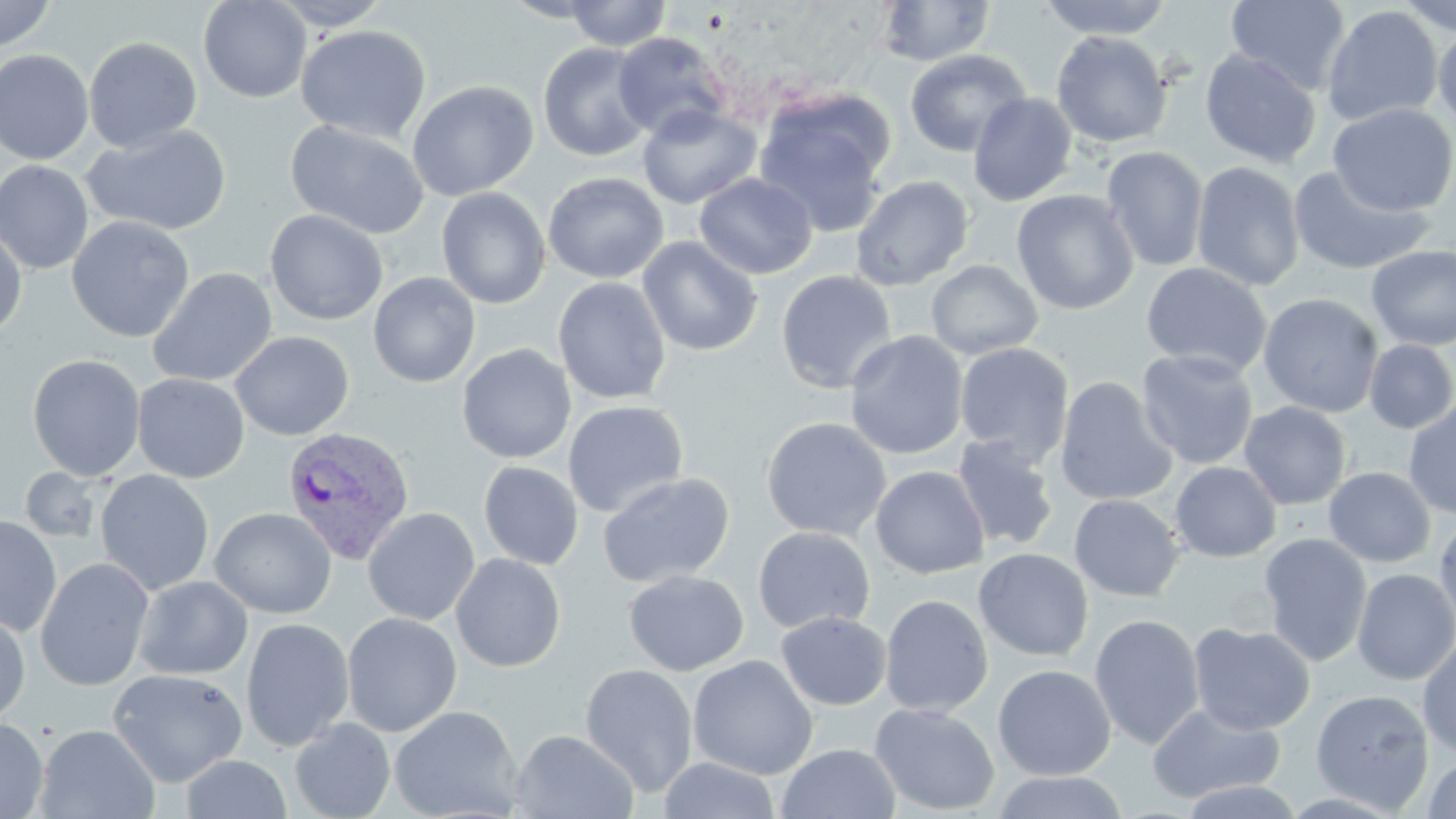
Plasmodium vivax-infected red blood cell locations = approximate bounding boxes as (x1, y1, x2, y2) in pixels: (282, 425, 415, 566)
slide-level diagnosis = Plasmodium vivax
stain = May-Grünwald-Giemsa
uninfected red blood cell locations = approximate bounding boxes as (x1, y1, x2, y2) in pixels: (0, 0, 59, 52), (198, 0, 311, 103), (268, 0, 393, 30), (562, 0, 672, 51), (1037, 0, 1174, 40), (1226, 0, 1351, 95), (1392, 0, 1456, 37), (876, 1, 997, 67), (1321, 5, 1443, 127), (1432, 21, 1456, 136), (295, 24, 432, 143), (1051, 30, 1172, 148), (612, 32, 731, 140), (83, 36, 202, 153), (537, 41, 655, 162), (904, 48, 1031, 158), (0, 49, 94, 165), (1200, 49, 1322, 168), (407, 80, 539, 201), (968, 92, 1078, 207), (753, 96, 892, 238), (637, 103, 761, 209), (1328, 103, 1456, 217), (285, 119, 431, 238), (81, 123, 232, 236), (1101, 146, 1209, 272), (0, 160, 94, 275), (1191, 161, 1305, 291), (1288, 165, 1435, 276), (543, 172, 668, 284), (694, 173, 817, 279), (850, 175, 974, 291), (436, 187, 551, 309), (1011, 189, 1139, 315), (264, 209, 388, 325), (66, 216, 195, 342), (0, 220, 28, 340), (637, 237, 763, 356), (1366, 245, 1456, 351), (926, 259, 1043, 360), (1141, 262, 1272, 377), (147, 267, 278, 387), (776, 270, 897, 394), (368, 272, 481, 388), (553, 276, 671, 404), (1258, 293, 1384, 418), (230, 330, 354, 441), (844, 330, 968, 460), (1363, 339, 1456, 434), (954, 342, 1075, 464), (457, 344, 576, 464), (1136, 349, 1259, 470), (27, 354, 145, 481), (132, 373, 249, 483), (1054, 376, 1178, 506), (562, 400, 689, 518), (1403, 400, 1456, 519), (1239, 401, 1352, 510), (760, 416, 891, 541), (949, 435, 1060, 552), (478, 460, 584, 570), (1170, 461, 1282, 562), (870, 465, 990, 579), (21, 467, 105, 544), (1323, 467, 1436, 567), (95, 469, 215, 596), (597, 472, 735, 589), (1069, 494, 1184, 602), (209, 507, 337, 619), (363, 507, 480, 625), (1434, 514, 1456, 634), (0, 516, 62, 636), (753, 526, 875, 633), (1258, 532, 1373, 666), (973, 548, 1094, 662), (450, 553, 566, 672), (35, 557, 155, 691), (1352, 568, 1456, 685), (623, 569, 749, 676), (133, 575, 253, 679), (879, 594, 993, 717), (0, 608, 30, 727), (776, 611, 891, 710), (342, 612, 462, 737), (1089, 613, 1205, 750), (240, 617, 355, 751), (1187, 622, 1315, 735), (1416, 634, 1456, 758), (688, 654, 818, 780), (579, 663, 699, 798), (993, 664, 1116, 780), (108, 668, 248, 787), (1311, 689, 1434, 814), (1146, 701, 1285, 804), (869, 702, 1000, 816), (389, 705, 524, 819), (290, 716, 395, 819), (0, 717, 48, 819), (35, 724, 161, 819), (510, 729, 638, 818), (776, 743, 902, 819), (180, 754, 292, 818), (1422, 756, 1456, 818), (657, 757, 782, 818), (990, 771, 1129, 818), (1174, 779, 1307, 818)
magnification = 1000x
preparation = thin blood smear
image size = 1456×819 pixels
modality = optical microscopy
field of view = one of a larger specimen